Comment on the morphology of the red blood cells.
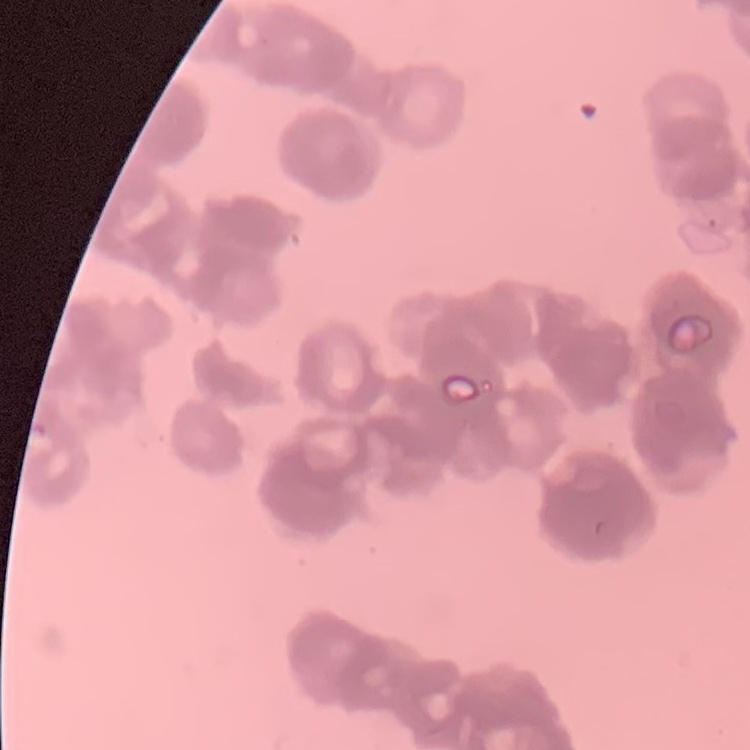

They show rouleaux formation.

preparation = thin blood film
stain = Field's or Giemsa
image type = one tile cut from a larger photomicrograph